Locate every malaria parasite.
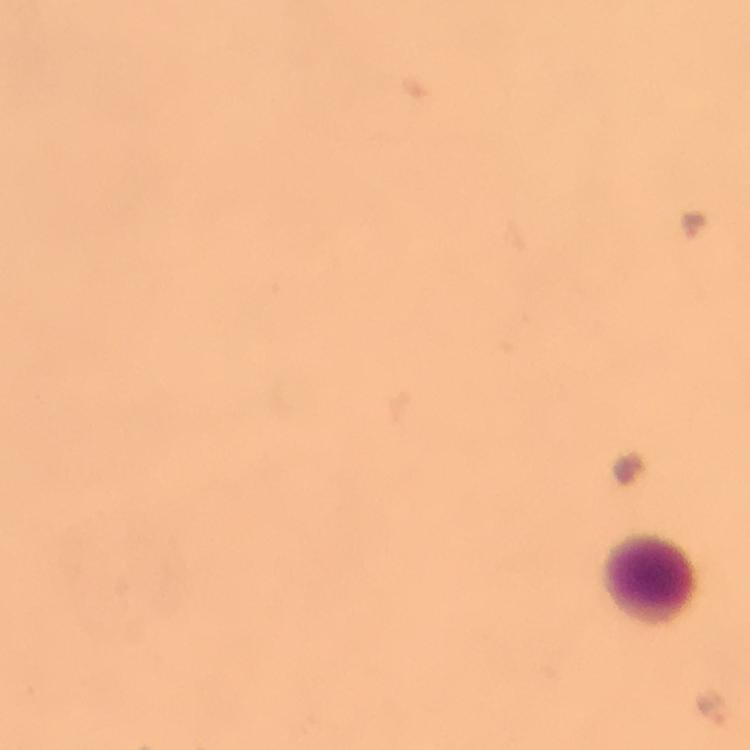

Approximate centers as [x, y] in pixels.
Malaria parasites: [693, 224], [714, 708].

{
  "image_size": "750×750 pixels",
  "cropped_from": "one field of view",
  "preparation": "thick smear",
  "magnification": "100x",
  "leukocyte_locations": "approximate centers as [x, y] in pixels: [650, 575]",
  "capture": "smartphone camera through the microscope",
  "immersion_oil": "used",
  "context": "from a malaria diagnostic workup",
  "stain": "Giemsa"
}